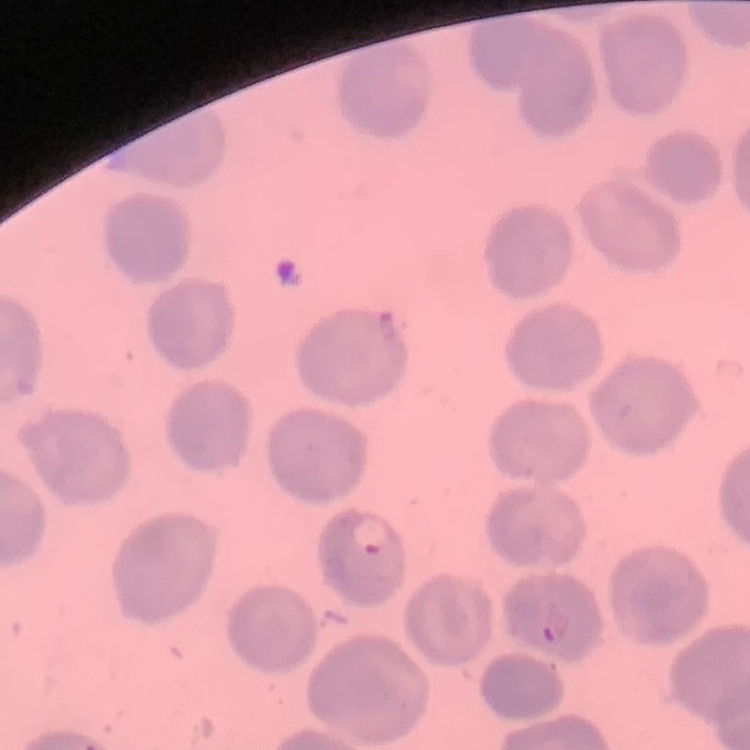
red blood cell morphology = no rouleaux formation
stain = Field's or Giemsa
image type = one tile cut from a larger photomicrograph
preparation = thin blood smear